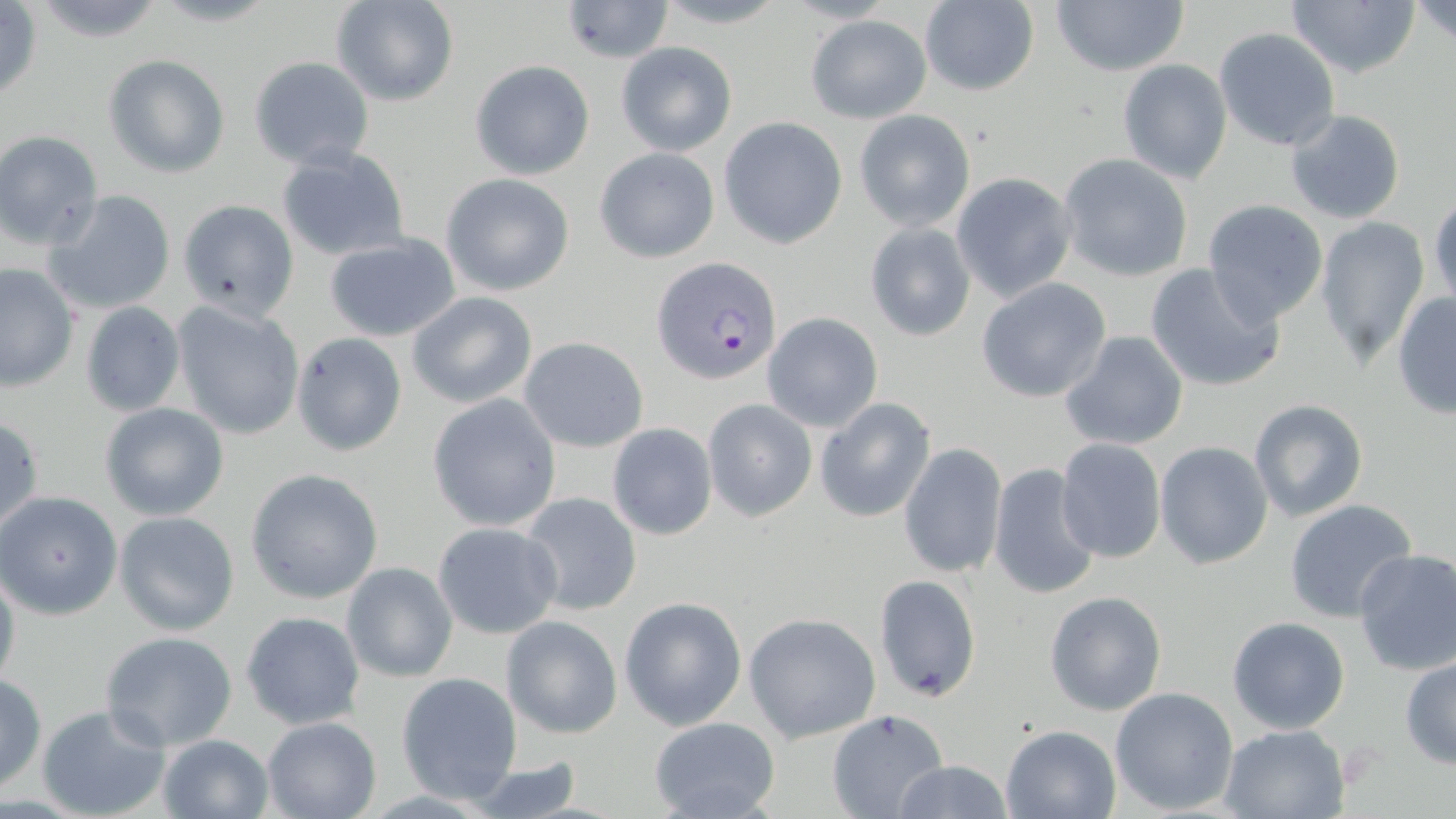

slide-level diagnosis = Plasmodium falciparum
field of view = single
modality = optical microscopy
stain = May-Grünwald-Giemsa
image size = 1456×819 pixels
preparation = thin blood smear
uninfected red blood cell locations = approximate bounding boxes as (x1, y1, x2, y2) in pixels: (1049, 0, 1189, 77), (1288, 0, 1419, 79), (1410, 0, 1456, 47), (29, 1, 171, 45), (330, 1, 460, 107), (560, 1, 676, 63), (917, 1, 1040, 98), (0, 2, 44, 107), (805, 13, 933, 123), (1213, 27, 1341, 152), (615, 41, 737, 157), (103, 53, 231, 178), (248, 56, 376, 169), (469, 59, 595, 180), (1116, 59, 1233, 184), (853, 110, 975, 231), (1283, 110, 1406, 226), (719, 117, 849, 250), (1, 131, 104, 249), (276, 145, 410, 264), (594, 146, 720, 263), (1057, 153, 1195, 283), (441, 172, 577, 297), (951, 172, 1076, 302), (43, 189, 177, 316), (1429, 195, 1455, 311), (1200, 198, 1329, 327), (177, 199, 299, 321), (1314, 216, 1430, 369), (864, 222, 976, 341), (322, 234, 462, 342), (0, 263, 78, 393), (1143, 263, 1286, 393), (976, 277, 1112, 403), (406, 291, 538, 407), (1391, 292, 1455, 418), (79, 301, 186, 417), (172, 301, 305, 441), (762, 312, 883, 432), (1058, 331, 1190, 453), (292, 332, 407, 457), (519, 337, 648, 452), (427, 394, 562, 533), (814, 397, 936, 523), (702, 398, 816, 522), (1247, 398, 1369, 522), (99, 401, 229, 521), (0, 414, 44, 539), (607, 423, 718, 540), (1054, 438, 1166, 564), (899, 442, 1008, 581), (1154, 442, 1272, 569), (988, 462, 1104, 602), (245, 468, 384, 605), (0, 490, 123, 619), (517, 491, 642, 616), (1283, 499, 1421, 623), (114, 510, 240, 636), (432, 521, 564, 639), (1351, 547, 1456, 676), (0, 561, 20, 695), (340, 561, 459, 683), (875, 573, 983, 703), (1045, 590, 1166, 717), (619, 596, 748, 730), (241, 611, 365, 729), (742, 612, 880, 743), (500, 613, 623, 739), (1227, 616, 1349, 734), (99, 632, 239, 750), (1401, 656, 1456, 770), (0, 672, 47, 794), (394, 672, 524, 804), (1108, 687, 1239, 813), (37, 704, 171, 819), (826, 709, 948, 819), (647, 716, 782, 819), (261, 717, 381, 819), (1218, 723, 1351, 817), (1000, 724, 1121, 818), (155, 733, 275, 819), (459, 758, 590, 819), (891, 760, 1015, 818)
magnification = 1000x
Plasmodium falciparum-infected red blood cell locations = approximate bounding boxes as (x1, y1, x2, y2) in pixels: (654, 257, 780, 385)